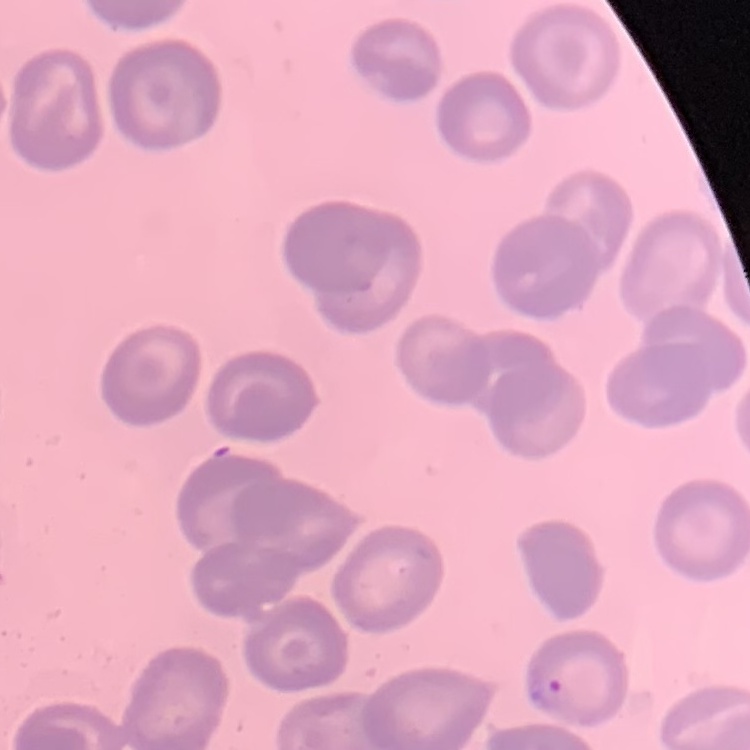

The erythrocytes exhibit no rouleaux formation. Field's or Giemsa stain. Thin peripheral smear. Square crop of a larger photomicrograph.